Classify this cell by malaria status.
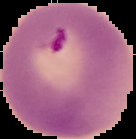

It is parasitized.

Summary:
  - Preparation: thin blood film
  - Image type: segmented cell region with the area outside set to black
  - Image size: 136×139 pixels